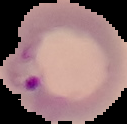
Image is 127×124 pixels. Result: Plasmodium parasites detected. Segmented cell region on a black background. From a thin blood smear.